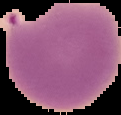

Summary:
  - Preparation: thin blood film
  - Image size: 121×115 pixels
  - Result: malaria parasites identified
  - Image type: cell region segmented out of the field of view; surrounding area masked to black